Comment on the morphology of the erythrocytes.
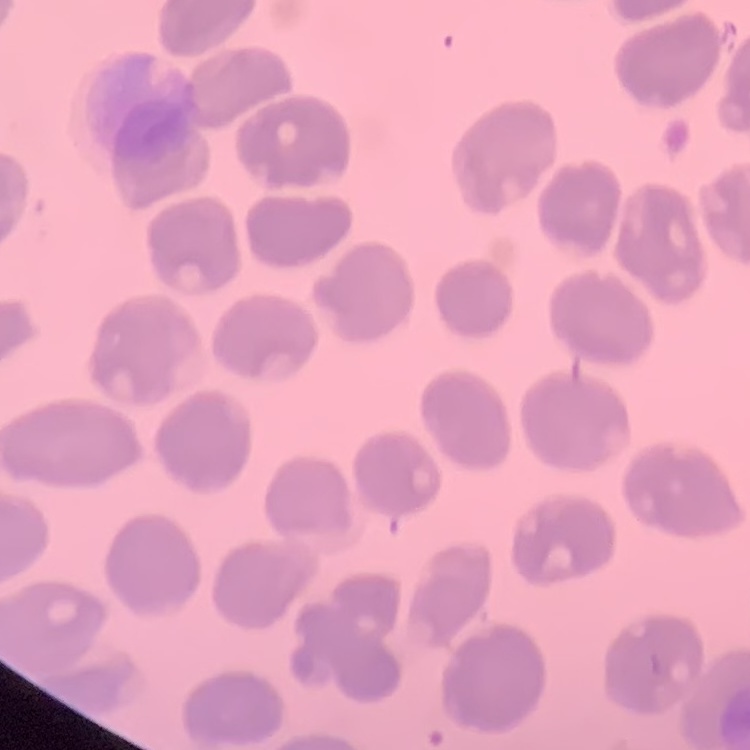
They show no rouleaux formation.

stain = Field's or Giemsa
image type = square crop of a larger photomicrograph
preparation = thin blood film